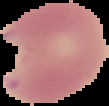
Summary:
  - Preparation: thin blood film
  - Result: malaria parasites identified
  - Image type: segmented cell region with the area outside set to black
  - Image size: 109×106 pixels